Identify the parasite.
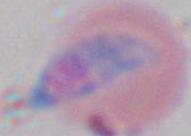
This is Toxoplasma gondii.

Captured at 1000x magnification. Micrograph.